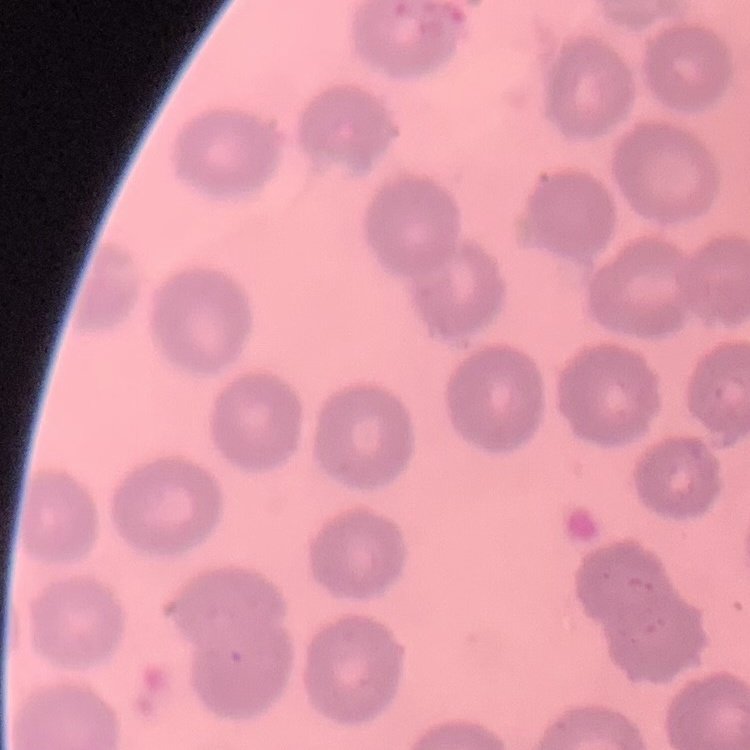

red blood cell morphology = no rouleaux formation
stain = Field's or Giemsa
preparation = thin blood film
image type = one tile cut from a larger photomicrograph